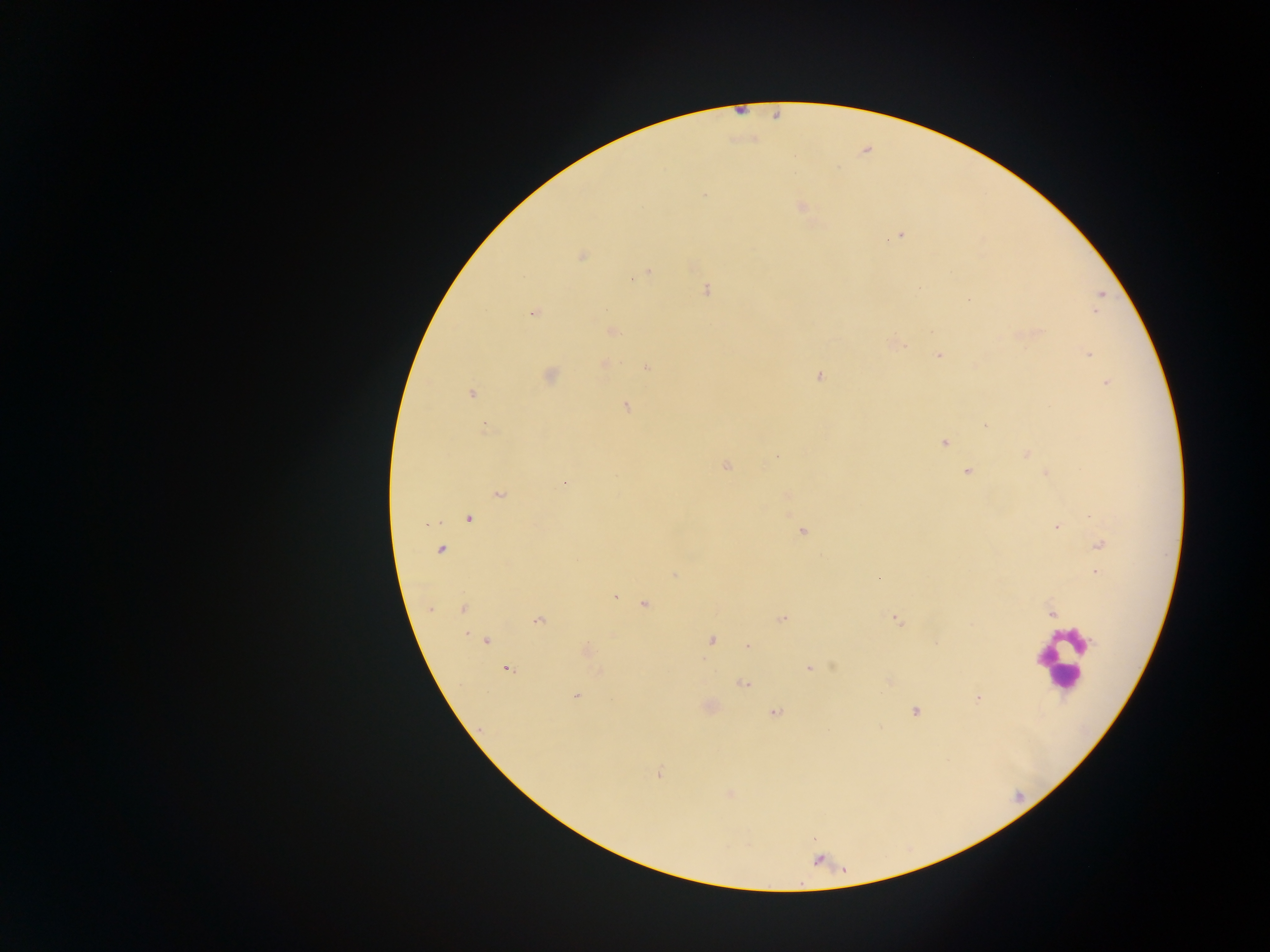
Approximate centers as {x, y} in pixels. Leukocyte locations: {1062, 661}. Malaria parasite locations: {801, 206}, {899, 234}, {581, 256}, {647, 272}, {706, 290}, {968, 298}, {533, 312}, {611, 331}, {896, 343}, {1087, 353}, {938, 355}, {604, 363}, {647, 367}, {549, 375}, {819, 375}, {1107, 382}, {470, 393}, {626, 406}, {986, 424}, {485, 426}, {944, 442}, {1026, 454}, {726, 465}, {967, 470}, {1047, 472}, {563, 484}, {498, 493}, {785, 494}, {468, 519}, {425, 523}, {1057, 526}, {802, 530}, {1099, 545}, {441, 550}, {674, 574}, {878, 577}, {613, 596}, {644, 604}, {463, 608}, {429, 609}, {1051, 611}, {782, 618}, {896, 619}, {538, 620}, {710, 639}, {486, 641}, {748, 646}, {585, 650}, {506, 668}, {808, 668}, {889, 680}, {743, 684}, {575, 696}, {977, 698}, {708, 707}, {915, 711}, {774, 712}, {658, 774}, {729, 792}. Photographed through a microscope with a mobile-phone camera. Single field of view. Image is 1270×952 pixels. Thick blood film. Collected in Ghana.